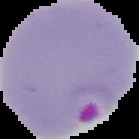

Summary:
  - Malaria status: parasitized
  - Image size: 139×139 pixels
  - Preparation: thin blood film
  - Image type: cell region segmented out of the field of view; surrounding area masked to black